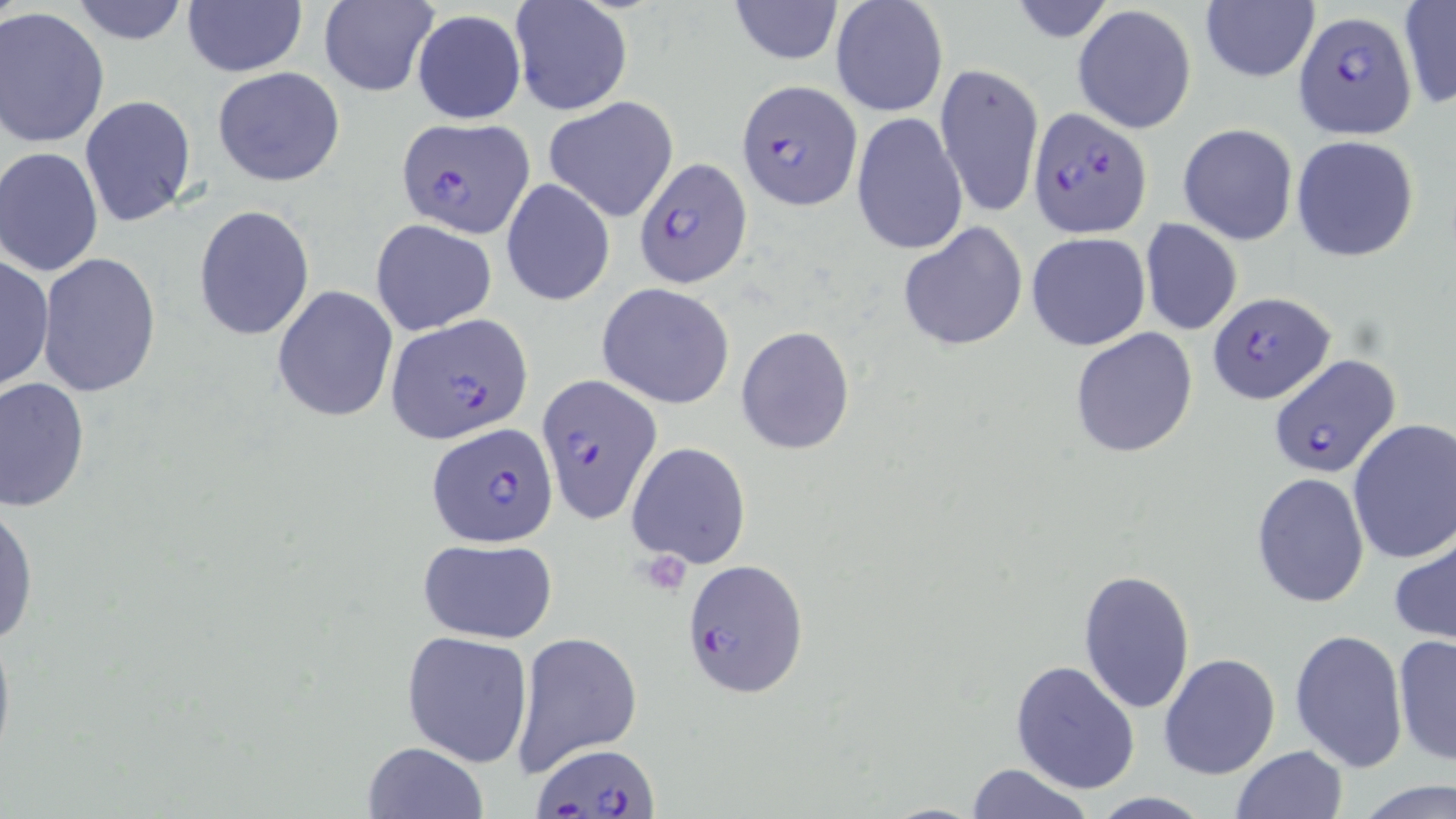

Approximate bounding boxes as (x1,y1)-(x2,y2) corner pairs in pixels. Plasmodium falciparum-infected red blood cell locations: (1295,12)-(1416,137), (736,80)-(863,211), (1027,106)-(1151,237), (396,117)-(533,238), (634,156)-(753,289), (1206,292)-(1335,404), (386,313)-(532,443), (1267,357)-(1396,477), (537,374)-(664,524), (427,423)-(559,547), (681,559)-(807,698), (535,744)-(660,816). Uninfected red blood cell locations: (68,0)-(190,45), (319,0)-(437,97), (510,0)-(633,116), (830,0)-(949,119), (1005,0)-(1119,44), (182,2)-(307,78), (728,2)-(843,66), (1199,2)-(1320,84), (1397,2)-(1455,110), (1072,4)-(1198,133), (1,8)-(111,148), (412,10)-(525,124), (934,61)-(1044,217), (213,67)-(345,188), (79,95)-(197,227), (543,97)-(680,222), (851,111)-(968,257), (1178,122)-(1299,246), (1290,134)-(1421,263), (0,147)-(104,277), (501,178)-(615,307), (193,204)-(315,341), (370,218)-(498,337), (1139,219)-(1242,337), (897,222)-(1027,353), (1026,232)-(1151,351), (37,252)-(161,397), (0,254)-(52,393), (596,283)-(735,410), (271,286)-(397,421), (736,326)-(855,455), (1070,328)-(1199,459), (0,375)-(90,512), (1347,419)-(1456,563), (627,441)-(751,569), (1250,472)-(1370,608), (0,502)-(37,648), (1389,528)-(1456,645), (416,539)-(558,642), (1076,569)-(1195,713), (0,613)-(16,772), (401,629)-(534,767), (1290,629)-(1409,772), (511,630)-(643,778), (1393,634)-(1456,765), (1158,652)-(1281,780), (1011,659)-(1142,795), (360,740)-(488,818), (1230,745)-(1347,819), (966,763)-(1095,818), (1354,781)-(1456,818), (1087,792)-(1213,818). Slide-level diagnosis: Plasmodium falciparum. Captured at 1000x magnification. May-Grünwald-Giemsa-stained preparation. Thin blood film. Optical microscopy. Single field of view. Image is 1456×819 pixels.